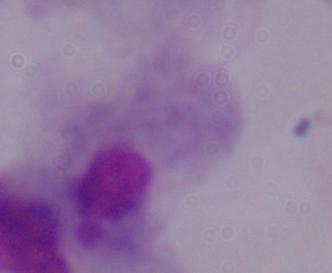
Summary:
  - Magnification: 1000x
  - Identification: trichomonad
  - Modality: photomicrograph